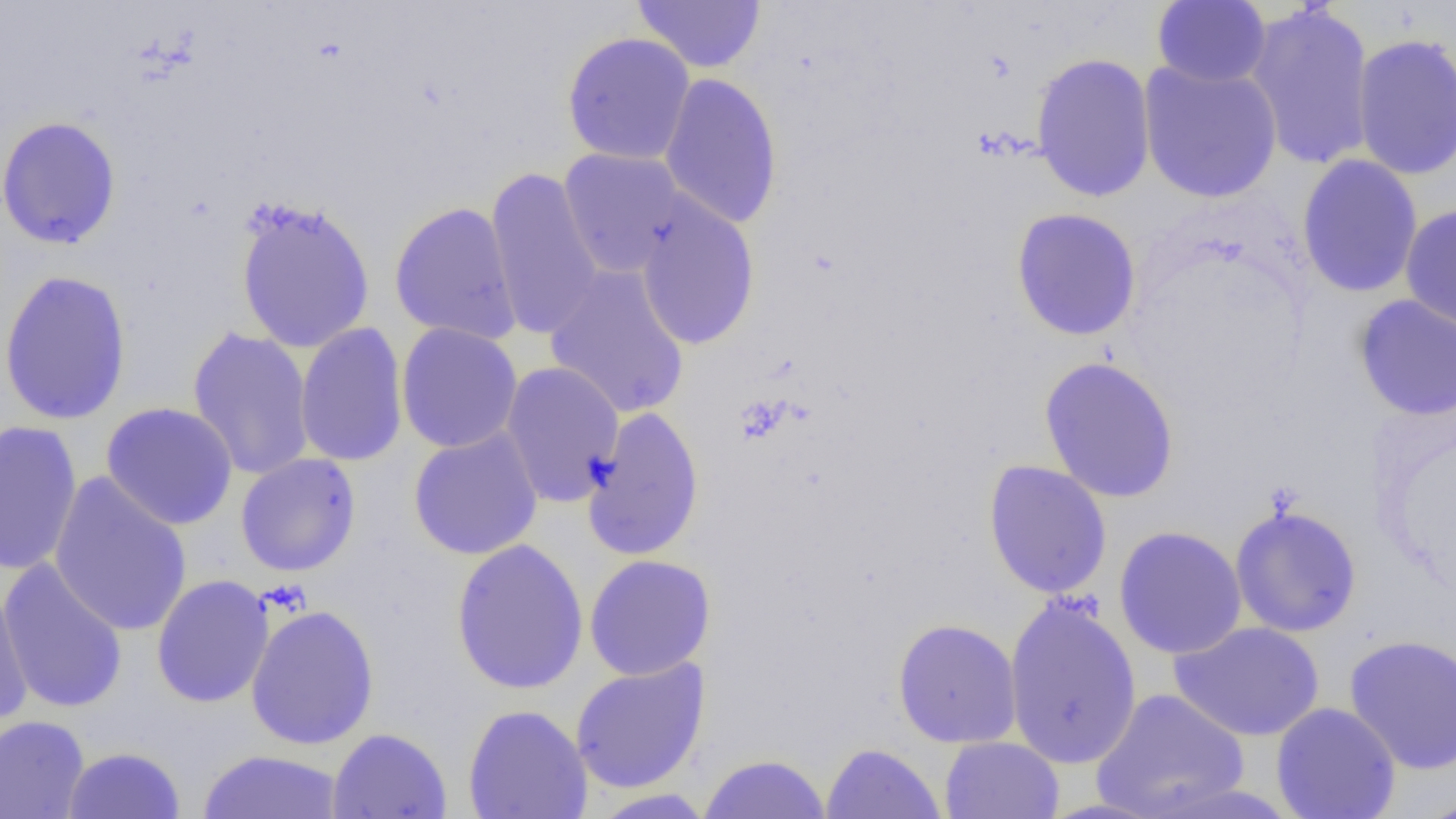
{
  "slide_level_diagnosis": "no evidence of blood parasites",
  "image_size": "1456×819 pixels",
  "magnification": "1000x",
  "preparation": "thin blood smear",
  "modality": "optical microscopy",
  "uninfected_red_blood_cell_locations": "approximate bounding boxes as (x1,y1)-(x2,y2) corner pairs in pixels: (632,1)-(766,73), (1151,1)-(1271,88), (1242,3)-(1376,171), (560,31)-(696,166), (1351,32)-(1456,180), (1030,52)-(1156,202), (1138,60)-(1282,204), (659,71)-(784,229), (0,116)-(122,250), (558,147)-(688,278), (1296,155)-(1423,299), (486,166)-(604,341), (634,194)-(760,351), (234,196)-(376,354), (389,201)-(522,345), (1399,204)-(1456,334), (1010,208)-(1142,342), (544,264)-(691,420), (0,269)-(133,426), (1353,293)-(1456,421), (295,322)-(409,468), (395,323)-(523,453), (186,326)-(315,480), (1039,356)-(1180,503), (500,361)-(625,506), (100,401)-(238,530), (582,406)-(705,562), (0,419)-(83,576), (408,427)-(544,561), (235,453)-(361,577), (983,460)-(1113,599), (48,472)-(193,637), (1229,504)-(1363,638), (1114,526)-(1247,660), (450,537)-(589,695), (584,554)-(716,681), (0,556)-(129,714), (151,574)-(274,708), (0,582)-(34,726), (1004,594)-(1143,769), (245,604)-(380,750), (893,618)-(1022,748), (1170,621)-(1325,741), (1343,633)-(1456,775), (570,657)-(710,794), (1091,688)-(1250,818), (1270,702)-(1401,819), (463,704)-(593,819), (0,715)-(90,819), (327,727)-(452,819), (939,736)-(1064,818), (820,742)-(945,819), (63,746)-(186,818), (197,749)-(345,818), (698,753)-(831,818), (588,788)-(716,818), (1414,791)-(1456,819)",
  "field_of_view": "one of a larger specimen"
}